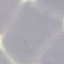

Result: negative for malaria parasites. Thin smear of blood. Photographed with a smartphone camera at the microscope eyepiece. Automatically extracted cell patch, resized to 64 × 64 pixels. Giemsa stain.